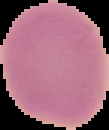

Summary:
  - Image type: segmented cell region on a black background
  - Image size: 109×130 pixels
  - Preparation: thin blood film
  - Result: no Plasmodium parasites seen